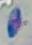

Summary:
  - Identification: Toxoplasma gondii
  - Magnification: 1000x
  - Modality: photomicrograph